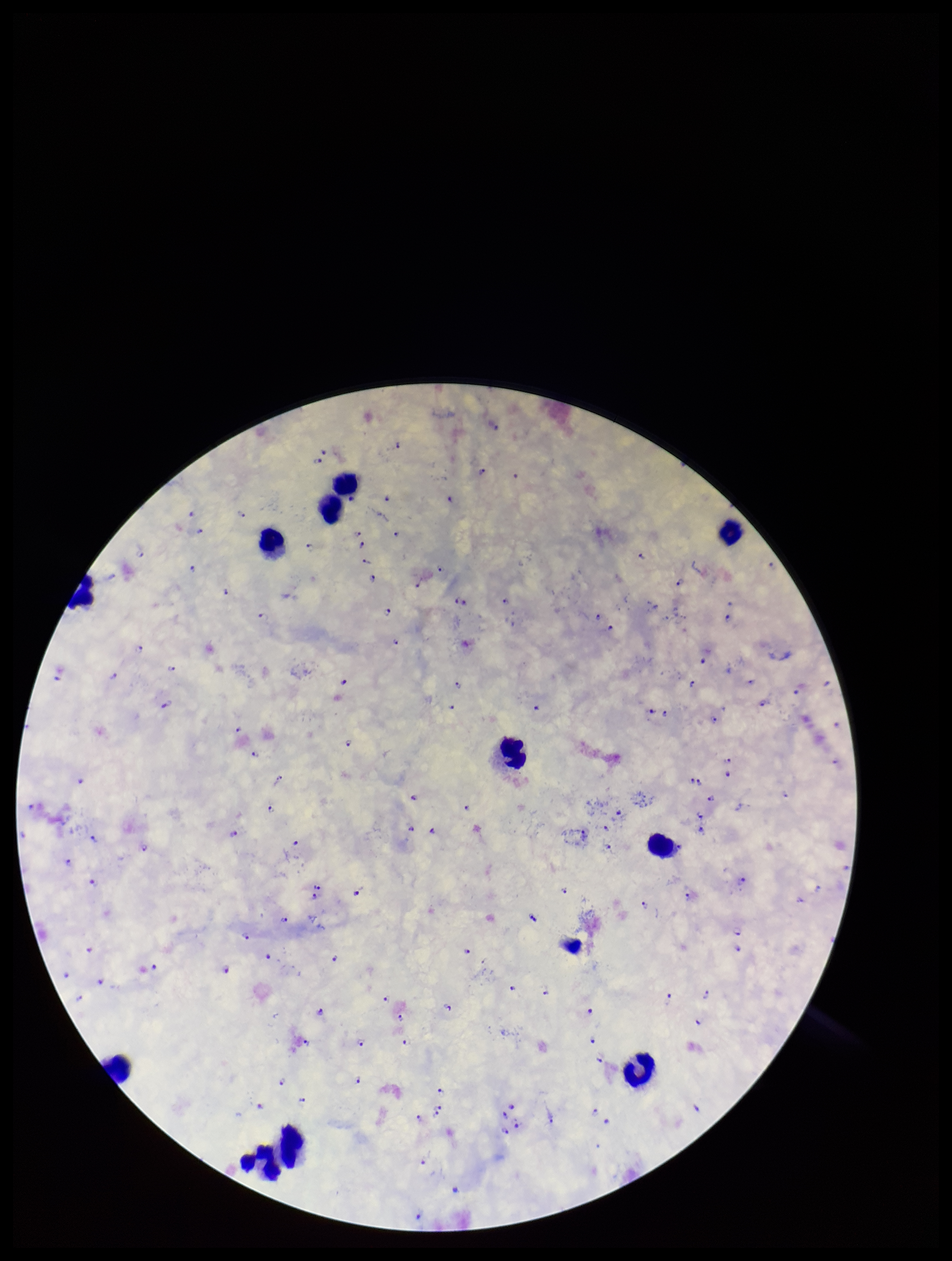
Summary:
  - Species reported for this patient: Plasmodium falciparum
  - Patient malaria status: positive
  - Image size: 952×1261 pixels
  - Field of view: one from this slide
  - Plasmodium parasites: identified
  - Leukocyte count: 11
  - Preparation: thick
  - Stain: Giemsa
  - Capture: smartphone photograph through the microscope eyepiece
  - Parasite count: 125